Comment on the morphology of the erythrocytes.
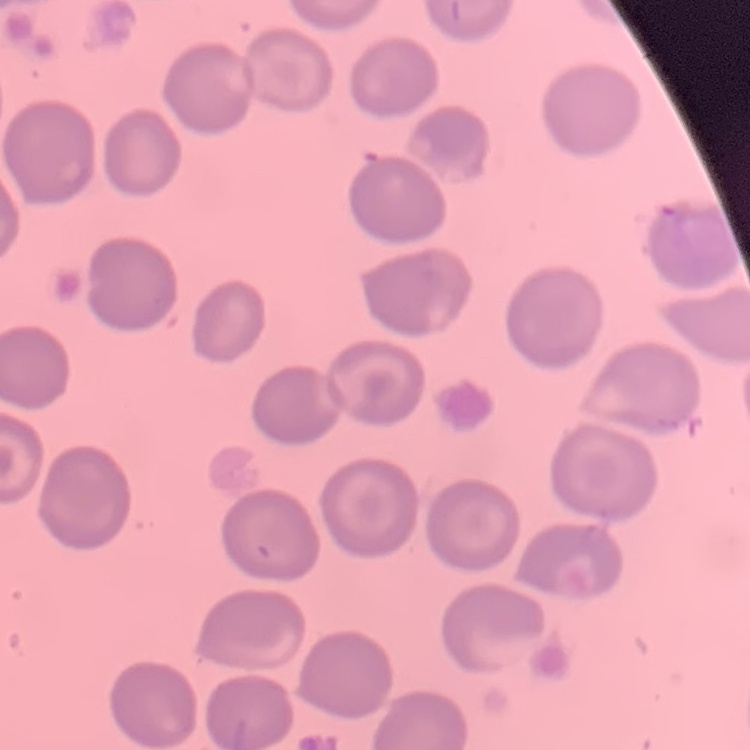

They show no rouleaux formation.

Summary:
  - Image type: square crop of a larger photomicrograph
  - Preparation: thin peripheral smear
  - Stain: Field's or Giemsa